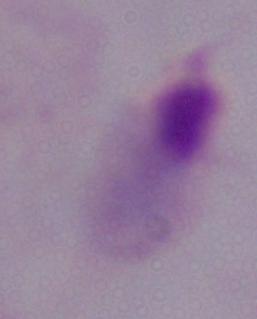
magnification = 1000x
identification = trichomonad
modality = photomicrograph